Give the position of every leukocyte visible.
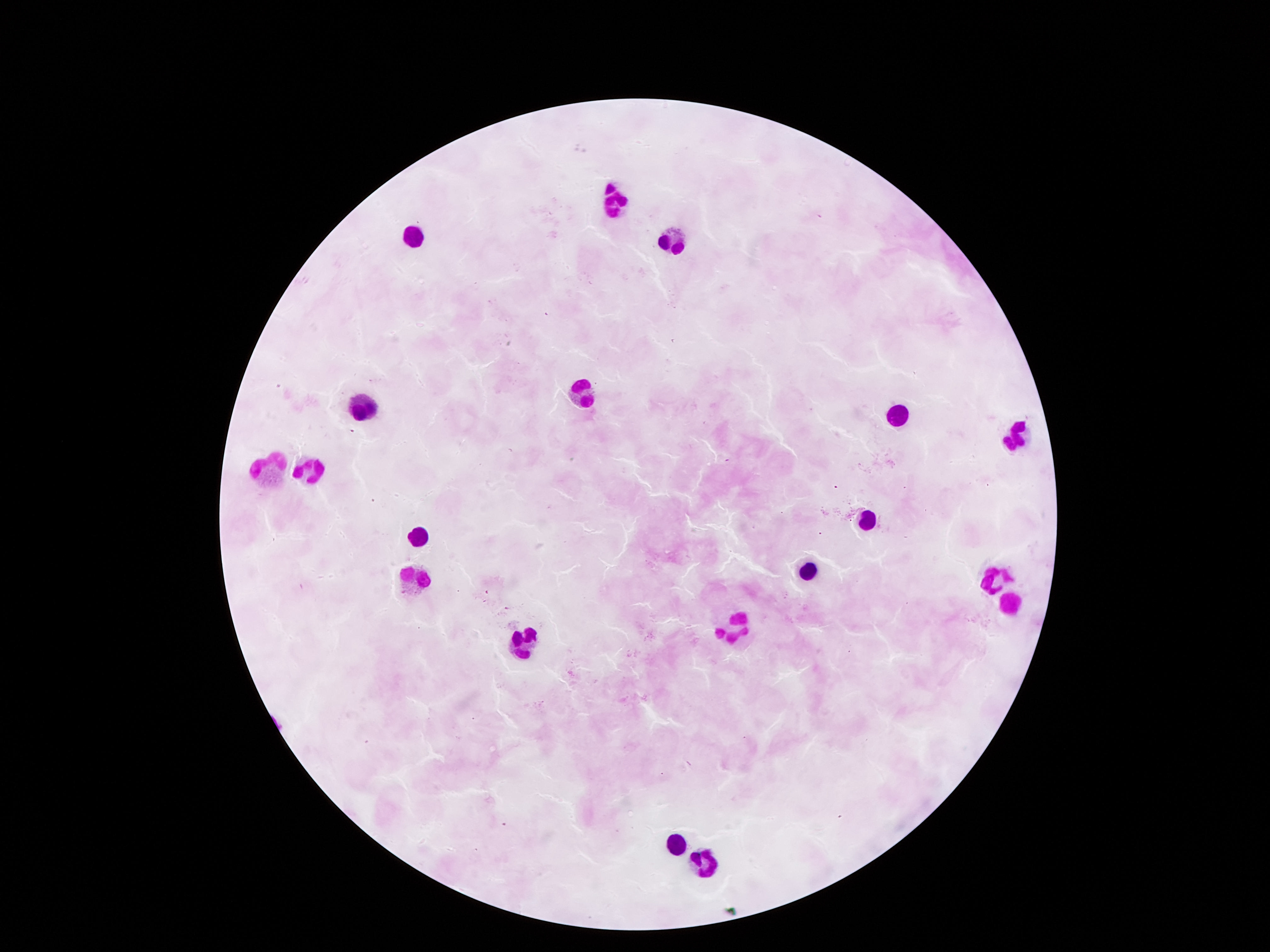

Approximate centers as (x, y) in pixels.
Leukocytes: (611, 204), (410, 240), (671, 240), (580, 393), (364, 404), (898, 412), (1009, 440), (264, 466), (306, 468), (871, 518), (412, 536), (806, 570), (411, 576), (998, 577), (1009, 606), (740, 626), (522, 642), (675, 843), (707, 861).

magnification = 100x
capture = smartphone camera through the microscope eyepiece
image size = 1270×952 pixels
patient malaria status = not infected
field of view = single
preparation = thick blood smear
stain = Giemsa